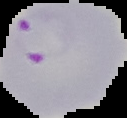

Summary:
  - Malaria status: parasitized
  - Image type: cell region segmented out of the field of view; surrounding area masked to black
  - Image size: 127×118 pixels
  - Preparation: thin blood film